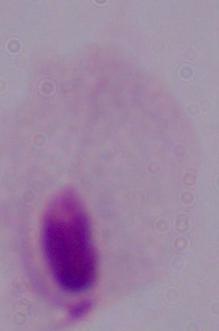

magnification = 1000x
identification = trichomonad
modality = micrograph